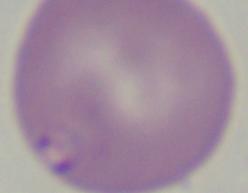

Summary:
  - Modality: photomicrograph
  - Identification: Babesia
  - Magnification: 1000x